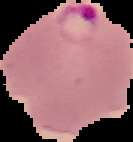

Malaria status: parasitized. Image is 133×142 pixels. The area outside the segmented cell region is set to black. From a thin blood smear.